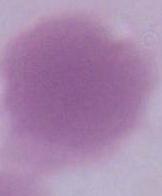

Summary:
  - Identification: red blood cell
  - Modality: photomicrograph
  - Magnification: 1000x